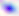

Summary:
  - Modality: micrograph
  - Identification: Toxoplasma gondii
  - Magnification: 400x